Assess this cell for malaria.
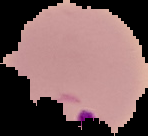
Parasitized.

Cell region segmented out of the field of view; the surrounding area is masked to black. Image is 148×136 pixels. From a thin blood film.